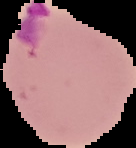
preparation = thin blood film
result = Plasmodium parasites detected
image type = segmented cell region with the area outside set to black
image size = 136×148 pixels